Name the cell type shown.
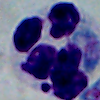

This is a leukocyte.

Photomicrograph. Captured at 1000x magnification.